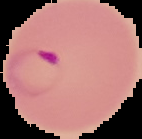
Image is 142×139 pixels. From a thin blood smear. Result: malaria parasites identified. Cell region segmented out of the field of view; the surrounding area is masked to black.